Report the malaria status of this cell.
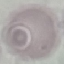

It is uninfected.

{
  "preparation": "thin smear",
  "stain": "Giemsa",
  "capture": "smartphone through the microscope eyepiece",
  "image_type": "automatically extracted cell patch, resized to 64 × 64 pixels"
}